Evaluate for malaria.
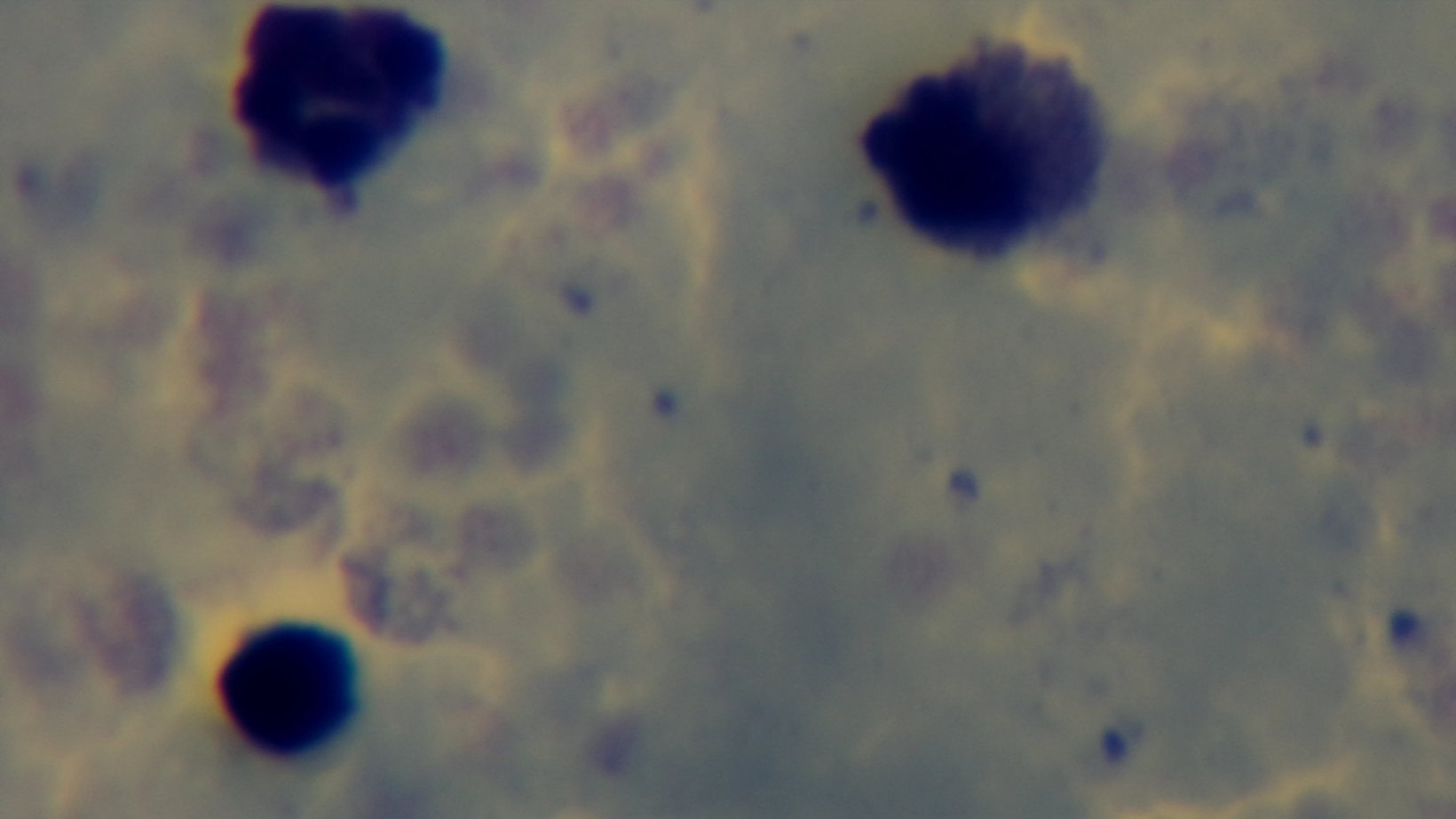

It is uninfected.

Summary:
  - Preparation: thick smear
  - Capture: mounted 4K digital camera
  - Stain: Giemsa
  - Field of view: one from the slide
  - Modality: light microscopy
  - Objective: 100x oil immersion